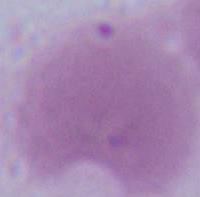

modality = photomicrograph
magnification = 1000x
identification = red blood cell